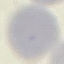
malaria status = uninfected
capture = smartphone through the microscope eyepiece
stain = Giemsa
image type = cell patch, automatically extracted from a larger field of view and resized to 64 × 64 pixels
preparation = thin blood film